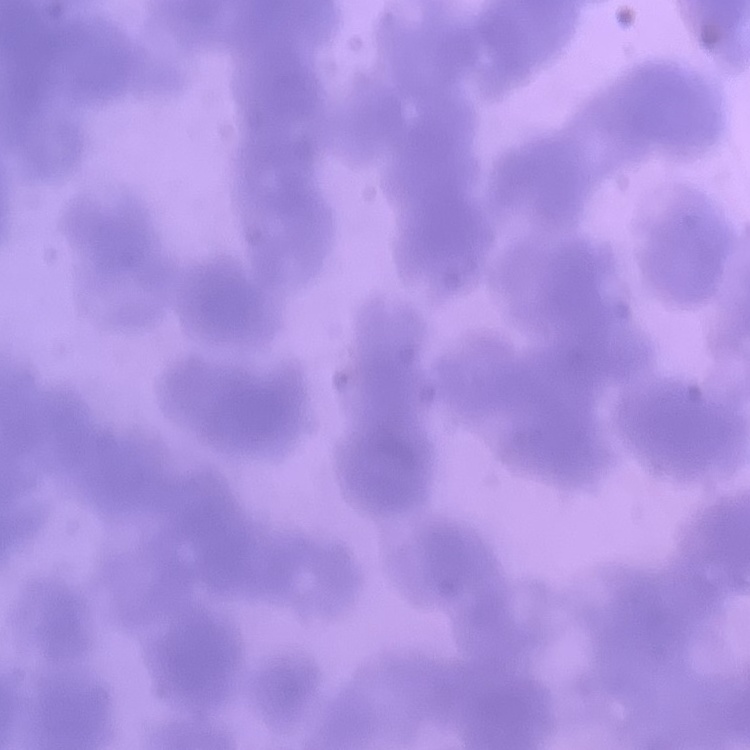
Summary:
  - Erythrocyte morphology: rouleaux formation
  - Preparation: thin blood smear
  - Image type: square crop of a larger photomicrograph
  - Stain: Field's or Giemsa